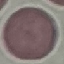
result = no malaria parasites seen
image type = automatically extracted cell patch, resized to 64 × 64 pixels
capture = smartphone through the microscope eyepiece
preparation = thin blood smear
stain = Giemsa